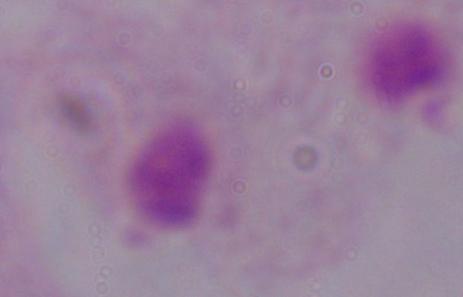

Summary:
  - Magnification: 1000x
  - Identification: trichomonad
  - Modality: photomicrograph